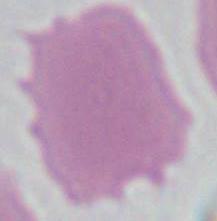
Summary:
  - Magnification: 1000x
  - Modality: photomicrograph
  - Identification: red blood cell